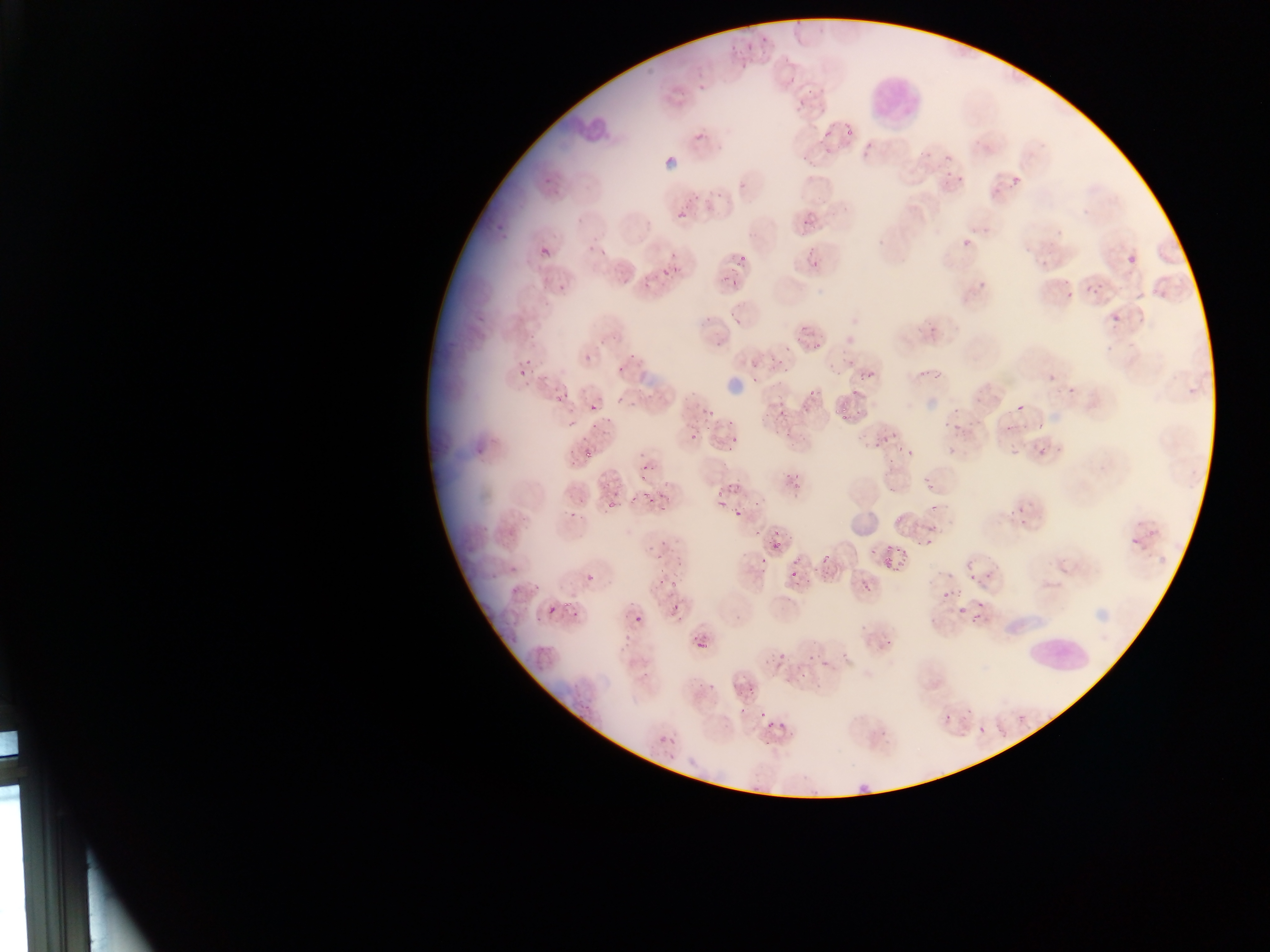

Approximate bounding boxes as (left, top, right, bottom) in pixels.
Summary:
  - Plasmodium parasite locations: (1012, 176, 1020, 185), (1082, 208, 1090, 216), (678, 211, 688, 220), (801, 221, 810, 229), (982, 227, 990, 235), (540, 245, 552, 258), (1025, 247, 1032, 255), (1128, 255, 1137, 264), (1038, 260, 1047, 270), (516, 365, 529, 378), (1048, 374, 1056, 382), (1016, 404, 1024, 412), (733, 509, 743, 519), (585, 573, 595, 583), (546, 603, 559, 616), (656, 735, 666, 745)
  - Image size: 1270×952 pixels
  - Field of view: single
  - Capture: mobile-phone photograph through a microscope
  - Preparation: thin blood smear
  - Country: Ghana